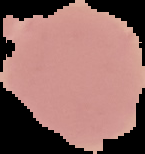
{
  "image_type": "segmented cell region with the area outside set to black",
  "result": "no Plasmodium parasites seen",
  "preparation": "thin blood film",
  "image_size": "145×154 pixels"
}